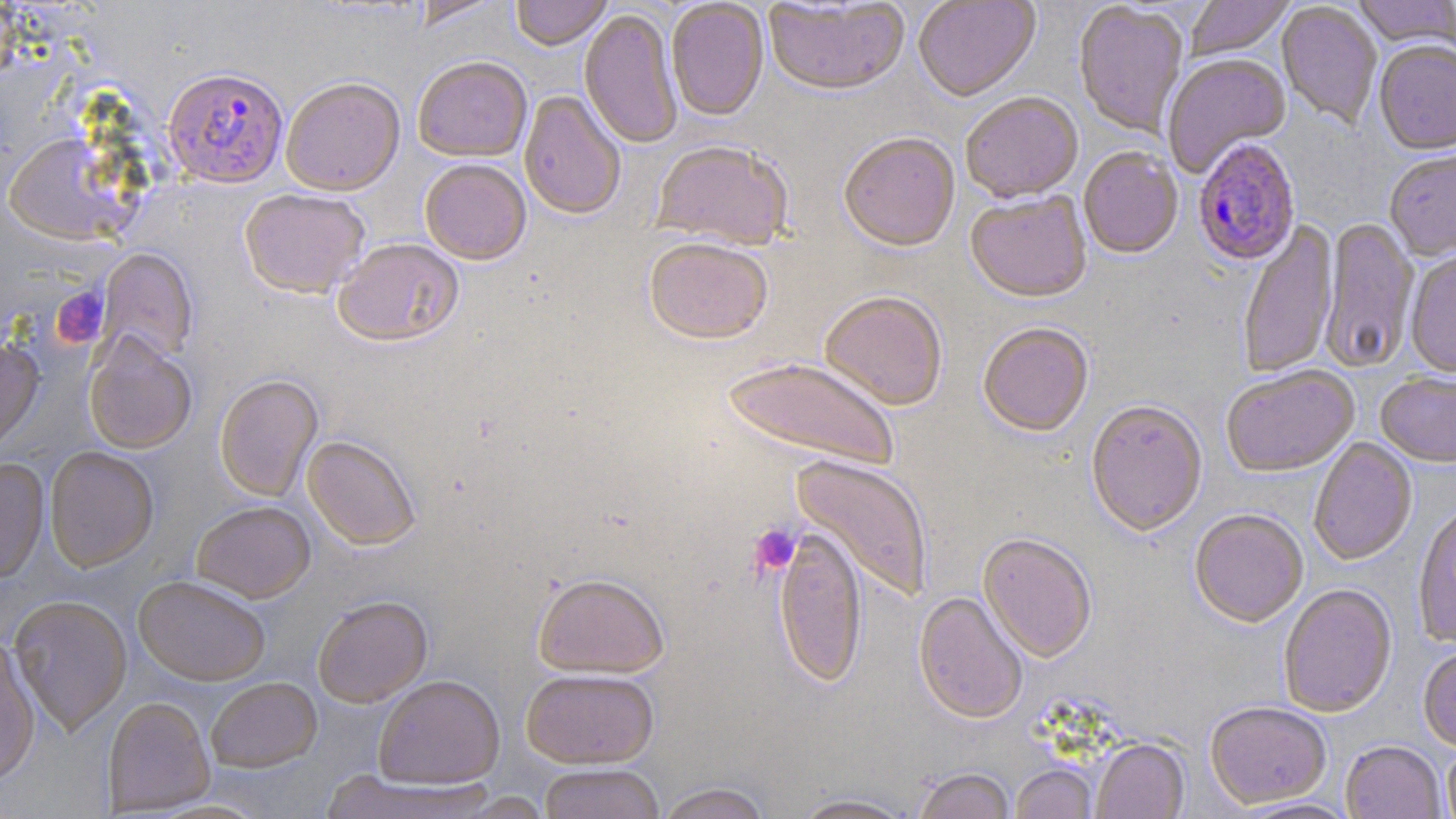 Approximate bounding boxes as [x1, y1, x2, y2] in pixels. Platelet locations: [52, 286, 109, 348], [748, 523, 802, 576]. Uninfected red blood cell locations: [408, 0, 504, 29], [510, 0, 612, 50], [763, 0, 911, 100], [913, 0, 1041, 104], [1186, 0, 1294, 61], [1352, 0, 1455, 51], [666, 1, 769, 121], [1276, 2, 1382, 130], [1074, 3, 1188, 139], [579, 9, 683, 149], [1374, 42, 1456, 158], [412, 55, 532, 161], [1163, 55, 1290, 178], [281, 76, 405, 194], [519, 90, 627, 219], [961, 94, 1084, 205], [3, 131, 132, 244], [838, 134, 961, 254], [651, 140, 794, 251], [1078, 148, 1183, 260], [1385, 151, 1456, 263], [419, 158, 531, 264], [239, 188, 370, 297], [965, 193, 1092, 305], [1319, 217, 1419, 374], [1238, 221, 1339, 380], [333, 237, 464, 346], [643, 238, 774, 345], [97, 248, 197, 363], [1405, 250, 1456, 380], [819, 292, 948, 412], [977, 325, 1094, 438], [83, 333, 197, 453], [0, 336, 43, 452], [722, 356, 900, 473], [1221, 367, 1360, 480], [214, 374, 322, 501], [1376, 374, 1456, 470], [1086, 402, 1208, 539], [303, 435, 421, 549], [1309, 438, 1418, 567], [45, 447, 158, 571], [791, 455, 933, 602], [0, 458, 49, 583], [192, 500, 315, 602], [1413, 506, 1456, 649], [1189, 511, 1307, 630], [773, 528, 867, 689], [977, 534, 1096, 664], [532, 572, 669, 678], [134, 575, 271, 685], [1279, 585, 1398, 719], [913, 592, 1028, 725], [8, 595, 132, 734], [312, 595, 432, 707], [0, 634, 41, 784], [1418, 647, 1456, 753], [521, 669, 659, 768], [373, 675, 504, 789], [206, 677, 322, 772], [103, 696, 214, 815], [1205, 703, 1332, 810], [1092, 739, 1189, 819], [1340, 742, 1446, 819], [1442, 743, 1456, 819], [538, 763, 665, 819], [1011, 765, 1098, 819], [912, 768, 1016, 819], [318, 769, 498, 818], [654, 783, 772, 819], [788, 793, 919, 818], [1233, 798, 1362, 818]. Plasmodium falciparum-infected red blood cell locations: [164, 66, 288, 187], [1192, 140, 1301, 268]. Slide-level diagnosis: Plasmodium falciparum. Captured at 1000x magnification. Image is 1456×819 pixels. May-Grünwald-Giemsa stain. One field of a larger specimen. Light microscopy. Thin blood smear.